Identify the preparation type.
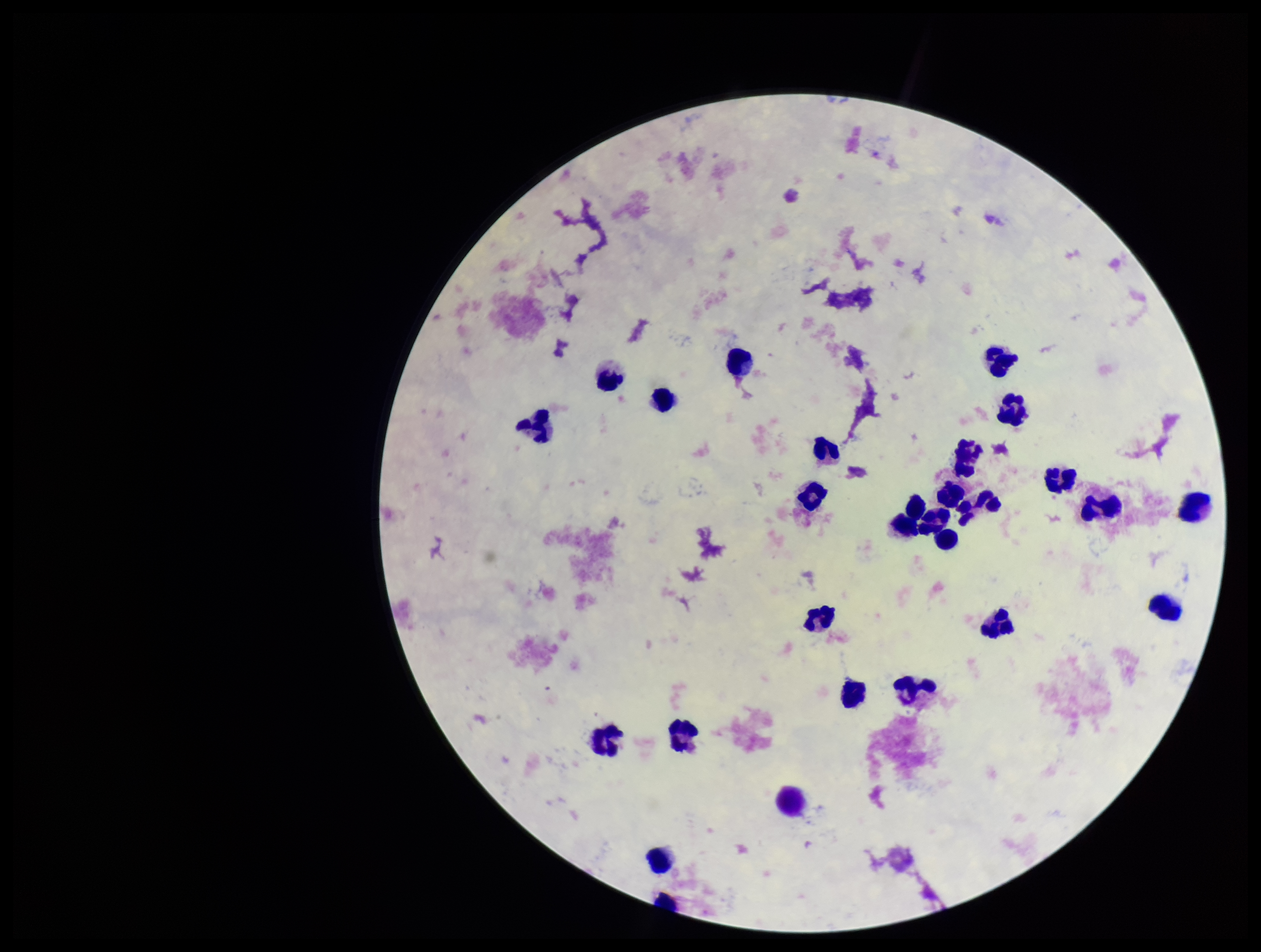
It is a thick blood smear.

Giemsa stain. Image is 1261×952 pixels. Photographed through the microscope eyepiece with a smartphone camera. Single field of view. Patient malaria status: negative. Leukocyte count: 29. Parasite count: 0. Plasmodium parasites: none detected.